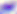
Summary:
  - Identification: Toxoplasma gondii
  - Magnification: 400x
  - Modality: micrograph